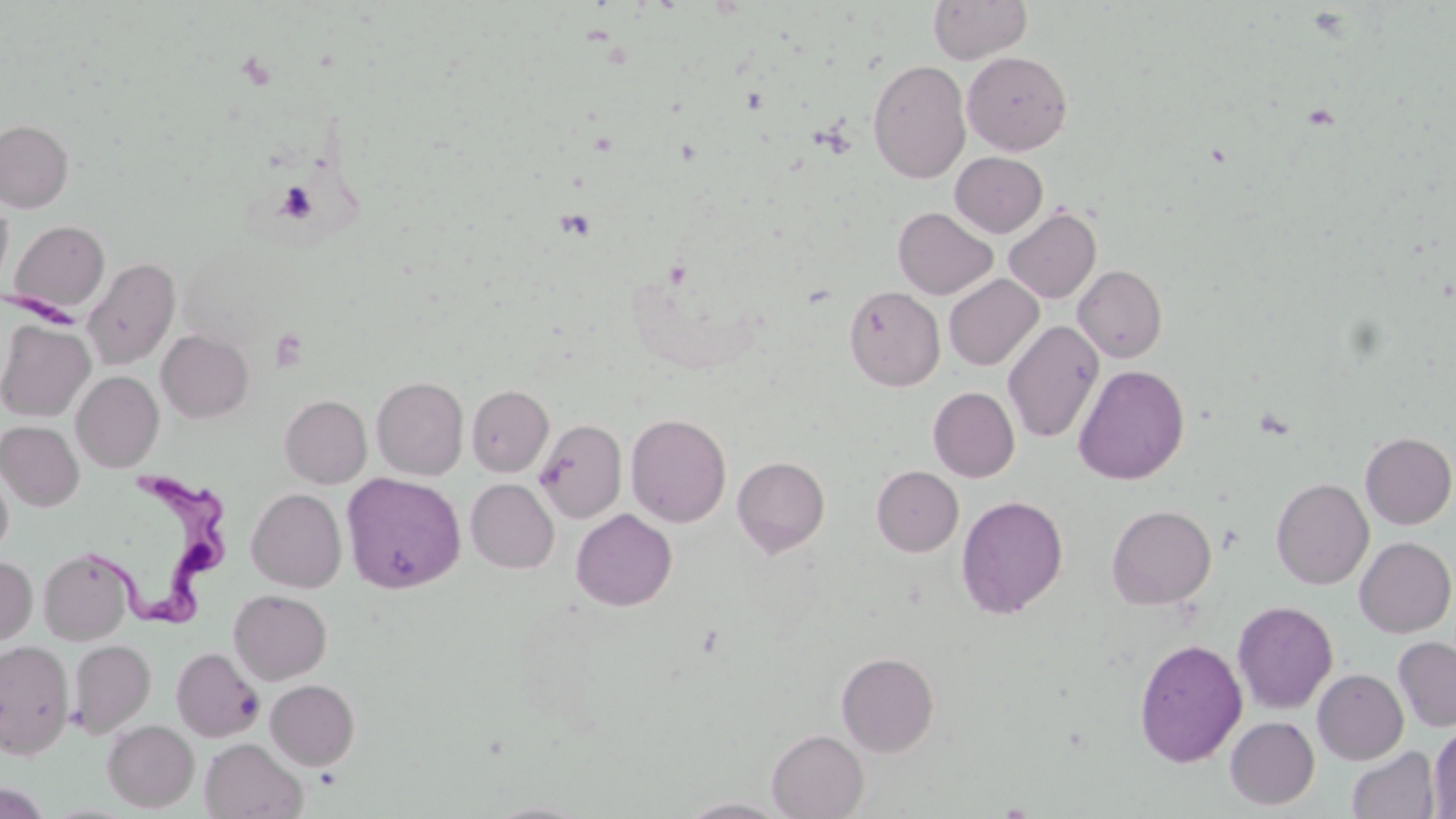

Summary:
  - Coordinate format: approximate bounding boxes as (x1, y1, x2, y2) in pixels
  - Platelet locations: (275, 182, 318, 223), (270, 329, 308, 371)
  - Trypanosoma brucei locations: (99, 472, 239, 629)
  - Uninfected red blood cell locations: (928, 0, 1032, 64), (962, 51, 1072, 156), (867, 59, 971, 183), (0, 119, 73, 213), (950, 152, 1048, 237), (0, 195, 13, 297), (893, 207, 998, 299), (1003, 207, 1101, 303), (9, 220, 109, 315), (83, 257, 180, 370), (1073, 265, 1168, 362), (944, 274, 1043, 371), (845, 286, 945, 392), (0, 320, 95, 421), (1003, 320, 1104, 444), (157, 330, 254, 423), (1073, 364, 1189, 485), (72, 371, 164, 473), (371, 376, 469, 480), (467, 385, 553, 477), (928, 387, 1020, 482), (280, 395, 371, 488), (626, 412, 731, 527), (534, 418, 626, 523), (1, 421, 84, 511), (1359, 432, 1456, 529), (732, 456, 830, 557), (0, 462, 13, 560), (872, 465, 963, 556), (341, 472, 465, 593), (1271, 477, 1373, 590), (466, 479, 559, 573), (247, 488, 346, 593), (955, 495, 1068, 618), (1106, 504, 1216, 610), (571, 509, 677, 610), (1354, 537, 1456, 637), (39, 547, 136, 644), (0, 557, 36, 647), (229, 589, 332, 684), (1232, 601, 1338, 714), (1393, 636, 1456, 733), (1134, 638, 1247, 767), (0, 639, 74, 758), (69, 639, 156, 737), (171, 647, 264, 742), (835, 651, 939, 756), (1313, 669, 1408, 765), (266, 679, 359, 770), (1225, 716, 1319, 810), (102, 719, 199, 812), (1428, 724, 1456, 818), (767, 729, 868, 818), (200, 739, 307, 819), (1347, 746, 1439, 819), (679, 797, 790, 818)
  - Slide-level diagnosis: Trypanosoma brucei
  - Field of view: one of a larger specimen
  - Magnification: 1000x
  - Image size: 1456×819 pixels
  - Modality: optical microscopy
  - Stain: May-Grünwald-Giemsa
  - Preparation: thin blood film